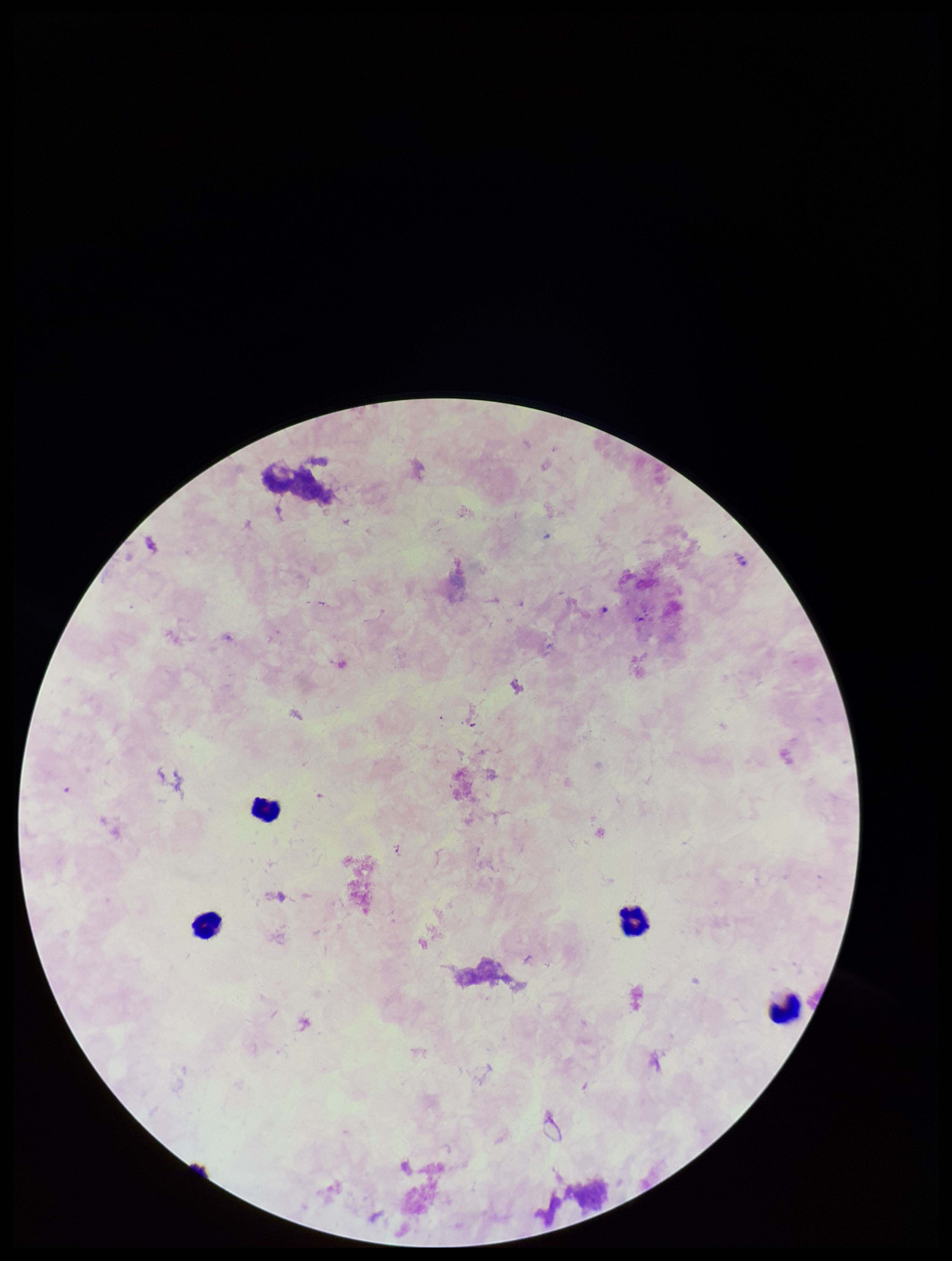 Preparation: thick. Giemsa stain. Plasmodium parasites: none identified. Photographed through the microscope eyepiece with a smartphone camera. Parasite count: 0. Leukocyte count: 4. Single field of view. Patient malaria status: negative. Image is 952×1261 pixels.